Report the malaria status of this cell.
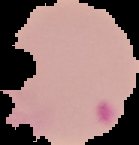

It is parasitized.

Summary:
  - Image size: 139×145 pixels
  - Image type: segmented cell region on a black background
  - Preparation: thin blood smear